Assess this cell for malaria.
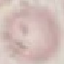
It is uninfected.

Summary:
  - Stain: Giemsa
  - Image type: cell patch, automatically extracted from a larger field of view and resized to 64 × 64 pixels
  - Capture: smartphone camera at the microscope eyepiece
  - Preparation: thin blood smear